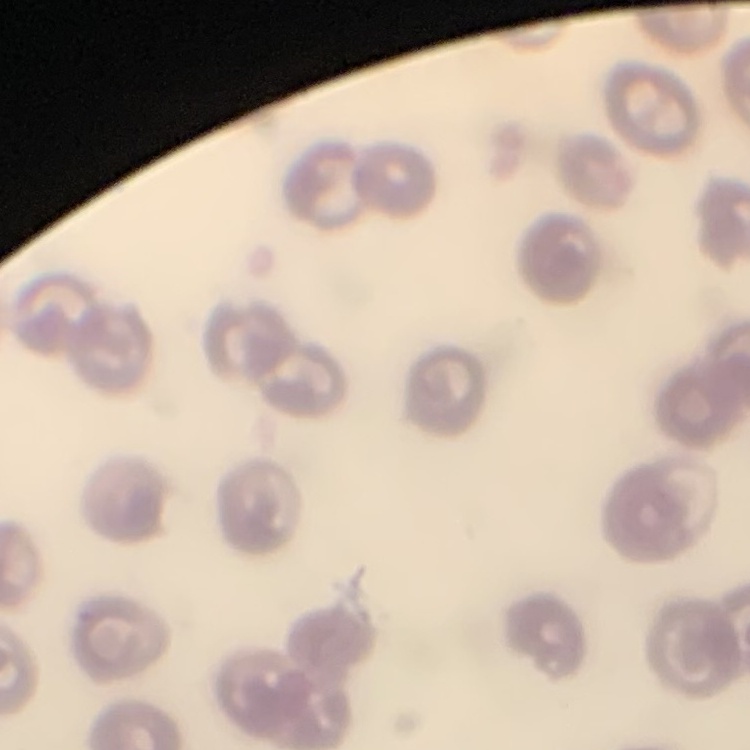
red blood cell morphology = no rouleaux formation
stain = Field's or Giemsa
image type = square crop of a larger photomicrograph
preparation = thin blood smear